Outline each Plasmodium ovale-infected red blood cell.
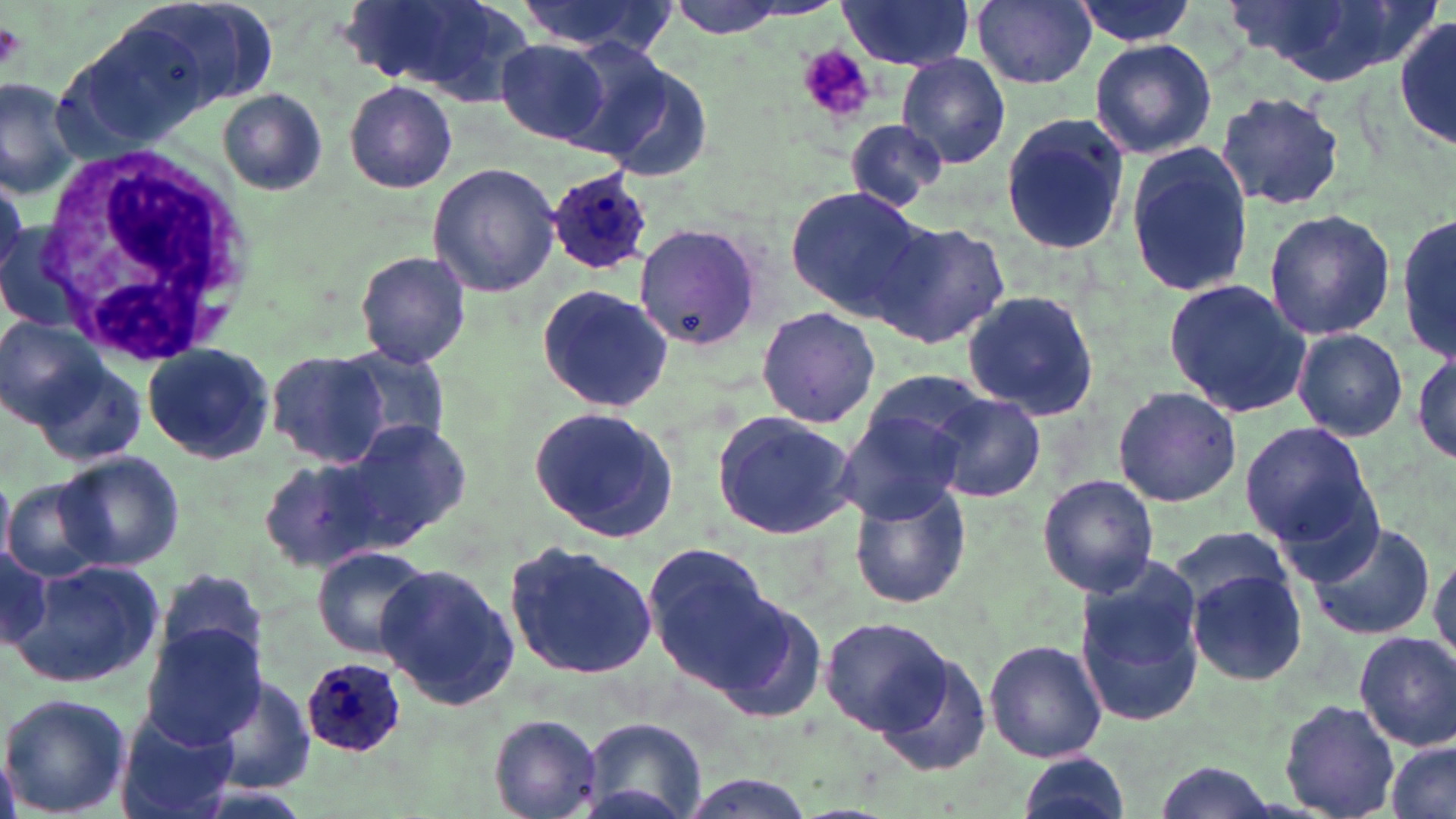

Approximate bounding boxes as (x1,y1)-(x2,y2) corner pairs in pixels.
Plasmodium ovale-infected red blood cells: (533,157)-(666,278), (299,658)-(407,756).

Uninfected red blood cell locations: (119,0)-(276,114), (514,0)-(678,57), (969,0)-(1098,89), (1071,0)-(1204,46), (1240,0)-(1420,86), (663,1)-(793,37), (836,1)-(976,70), (340,2)-(522,95), (1393,13)-(1456,150), (1089,38)-(1216,160), (499,39)-(613,144), (897,52)-(1011,168), (592,55)-(714,180), (0,74)-(83,199), (345,81)-(457,194), (217,88)-(327,196), (1214,91)-(1348,211), (999,111)-(1133,257), (842,119)-(948,209), (1125,142)-(1256,301), (427,163)-(559,297), (784,188)-(933,323), (1263,208)-(1394,341), (1396,211)-(1455,366), (872,219)-(1010,350), (629,225)-(765,352), (355,249)-(471,367), (1164,277)-(1314,417), (537,283)-(674,413), (961,290)-(1104,421), (756,306)-(881,429), (0,317)-(106,427), (1291,328)-(1410,442), (335,342)-(448,452), (141,343)-(276,464), (1412,348)-(1456,465), (266,349)-(393,467), (37,362)-(145,467), (858,368)-(988,469), (1114,385)-(1243,506), (932,393)-(1046,502), (528,405)-(680,544), (838,406)-(972,525), (710,410)-(858,540), (340,418)-(472,544), (1239,422)-(1375,548), (59,452)-(184,571), (258,457)-(385,573), (1037,474)-(1161,597), (0,478)-(15,569), (4,479)-(106,582), (847,479)-(972,610), (1304,516)-(1436,641), (1169,526)-(1299,626), (505,540)-(660,681), (643,542)-(775,686), (314,547)-(435,659), (1429,547)-(1456,670), (0,551)-(52,651), (12,561)-(164,692), (376,561)-(520,710), (1072,562)-(1206,729), (155,566)-(269,674), (1186,569)-(1310,686), (709,595)-(830,725), (819,614)-(954,735), (140,625)-(264,748), (1354,631)-(1456,750), (985,638)-(1109,762), (868,646)-(996,780), (207,671)-(317,795), (0,691)-(130,817), (1280,699)-(1398,817), (114,714)-(236,819), (490,714)-(602,817), (579,718)-(709,819), (1385,739)-(1455,819), (1014,753)-(1130,819), (671,774)-(819,817). Platelet locations: (0,21)-(25,72), (794,46)-(881,125). White blood cell locations: (32,144)-(252,363). Slide-level diagnosis: Plasmodium ovale. May-Grünwald-Giemsa-stained preparation. Thin blood smear. Single field of view. Image is 1456×819 pixels. Captured at 1000x magnification. Optical microscopy.